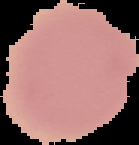
Result: no Plasmodium parasites detected. Image is 139×145 pixels. Cell region segmented out of the field of view; the surrounding area is masked to black. From a thin blood smear.